Give the position of every Plasmodium parasite.
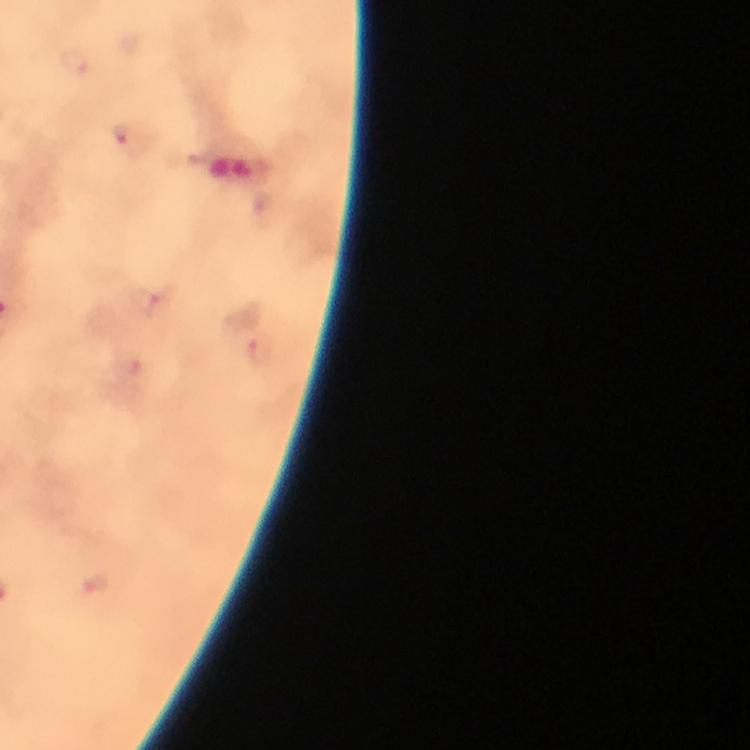

Approximate centers as (x, y) in pixels.
Plasmodium parasites: (75, 60), (129, 136), (148, 300), (262, 349), (95, 584).

Photographed through the microscope with a smartphone camera. From a diagnostic examination for malaria. 100x magnification. A crop from one field of view. Thick blood film. Image is 750×750 pixels. Giemsa stain. Immersion oil applied.